Report the malaria status of this cell.
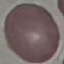

Uninfected.

Summary:
  - Stain: Giemsa
  - Preparation: thin smear
  - Capture: smartphone camera at the microscope eyepiece
  - Image type: cell patch, automatically extracted from a larger field of view and resized to 64 × 64 pixels